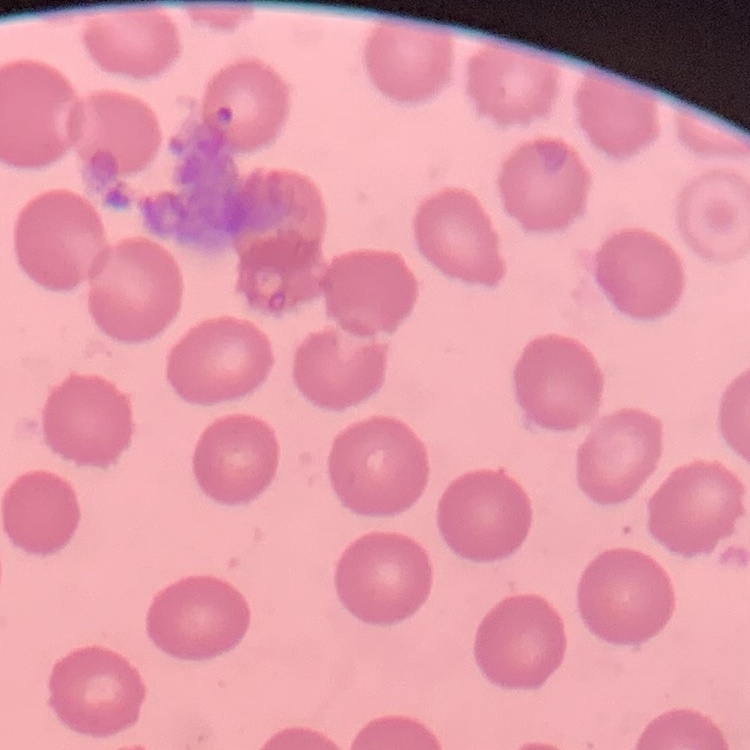
The red blood cells exhibit no rouleaux formation. Thin blood film. One tile cut from a larger photomicrograph. Field's or Giemsa stain.